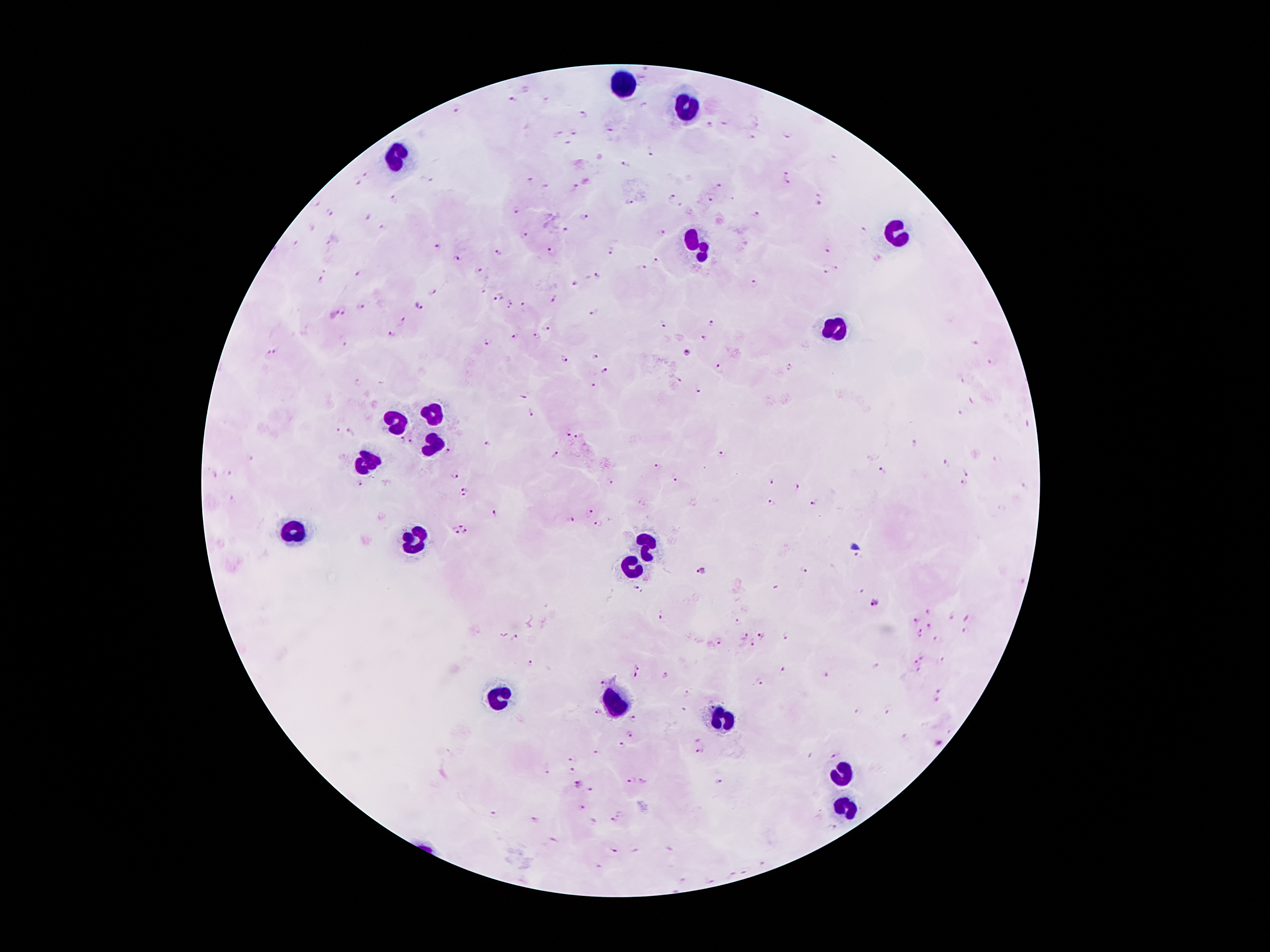

Approximate centers as {x, y} in pixels. Malaria parasite locations: {512, 100}, {546, 101}, {642, 104}, {457, 108}, {584, 113}, {724, 123}, {709, 126}, {611, 131}, {574, 132}, {559, 133}, {788, 137}, {751, 138}, {568, 142}, {648, 153}, {626, 165}, {782, 170}, {366, 174}, {426, 180}, {529, 181}, {357, 182}, {788, 184}, {719, 187}, {573, 188}, {546, 189}, {817, 195}, {670, 197}, {394, 199}, {711, 200}, {629, 202}, {818, 203}, {517, 211}, {329, 213}, {756, 216}, {367, 217}, {585, 218}, {382, 226}, {568, 229}, {861, 231}, {659, 233}, {524, 236}, {327, 242}, {298, 243}, {438, 246}, {500, 251}, {553, 251}, {827, 251}, {610, 253}, {457, 260}, {657, 260}, {836, 265}, {642, 270}, {479, 272}, {825, 272}, {357, 275}, {598, 276}, {321, 278}, {575, 283}, {755, 284}, {483, 290}, {432, 291}, {498, 296}, {556, 299}, {510, 305}, {524, 305}, {419, 306}, {364, 308}, {594, 313}, {334, 314}, {710, 322}, {401, 323}, {662, 324}, {549, 329}, {392, 334}, {516, 336}, {537, 336}, {704, 337}, {488, 343}, {974, 344}, {344, 345}, {279, 350}, {687, 353}, {265, 354}, {594, 355}, {564, 360}, {990, 363}, {718, 368}, {791, 368}, {604, 370}, {678, 380}, {960, 382}, {358, 383}, {593, 385}, {698, 389}, {524, 396}, {531, 413}, {959, 413}, {338, 430}, {349, 431}, {567, 431}, {576, 436}, {401, 441}, {411, 443}, {487, 443}, {913, 444}, {447, 451}, {555, 454}, {722, 455}, {251, 460}, {996, 460}, {947, 463}, {657, 466}, {880, 471}, {453, 473}, {965, 474}, {227, 475}, {675, 479}, {610, 480}, {768, 480}, {359, 483}, {963, 484}, {795, 487}, {1024, 487}, {464, 493}, {230, 499}, {771, 503}, {812, 503}, {493, 510}, {591, 510}, {569, 520}, {599, 523}, {460, 526}, {457, 533}, {465, 533}, {856, 556}, {803, 569}, {701, 571}, {634, 586}, {861, 591}, {873, 604}, {929, 609}, {660, 615}, {950, 617}, {968, 619}, {737, 622}, {917, 622}, {928, 627}, {920, 632}, {761, 637}, {785, 637}, {744, 638}, {516, 639}, {938, 639}, {717, 644}, {753, 645}, {923, 657}, {915, 660}, {941, 661}, {531, 663}, {638, 667}, {876, 667}, {783, 668}, {919, 672}, {665, 674}, {634, 675}, {827, 675}, {763, 680}, {603, 681}, {938, 691}, {687, 696}, {937, 701}, {598, 711}, {886, 711}, {856, 712}, {633, 719}, {631, 733}, {696, 740}, {939, 744}, {623, 745}, {699, 752}, {598, 754}, {833, 756}, {573, 759}, {547, 771}, {573, 771}, {631, 780}, {642, 780}, {720, 782}, {578, 784}, {591, 790}, {579, 807}, {495, 814}, {614, 819}, {535, 820}, {593, 821}, {834, 826}, {551, 841}, {612, 850}, {764, 863}, {744, 872}, {731, 874}, {681, 879}, {711, 880}. Leukocyte locations: {620, 81}, {685, 110}, {392, 159}, {892, 233}, {695, 248}, {829, 329}, {433, 415}, {398, 422}, {434, 440}, {368, 462}, {292, 532}, {415, 540}, {644, 547}, {631, 567}, {500, 695}, {616, 700}, {722, 722}, {841, 774}, {850, 809}. One field from this slide. 100x magnification. Image is 1270×952 pixels. Photographed through the microscope eyepiece with a smartphone camera. Giemsa-stained preparation. Patient malaria status: infected with Plasmodium falciparum. Thick blood film.